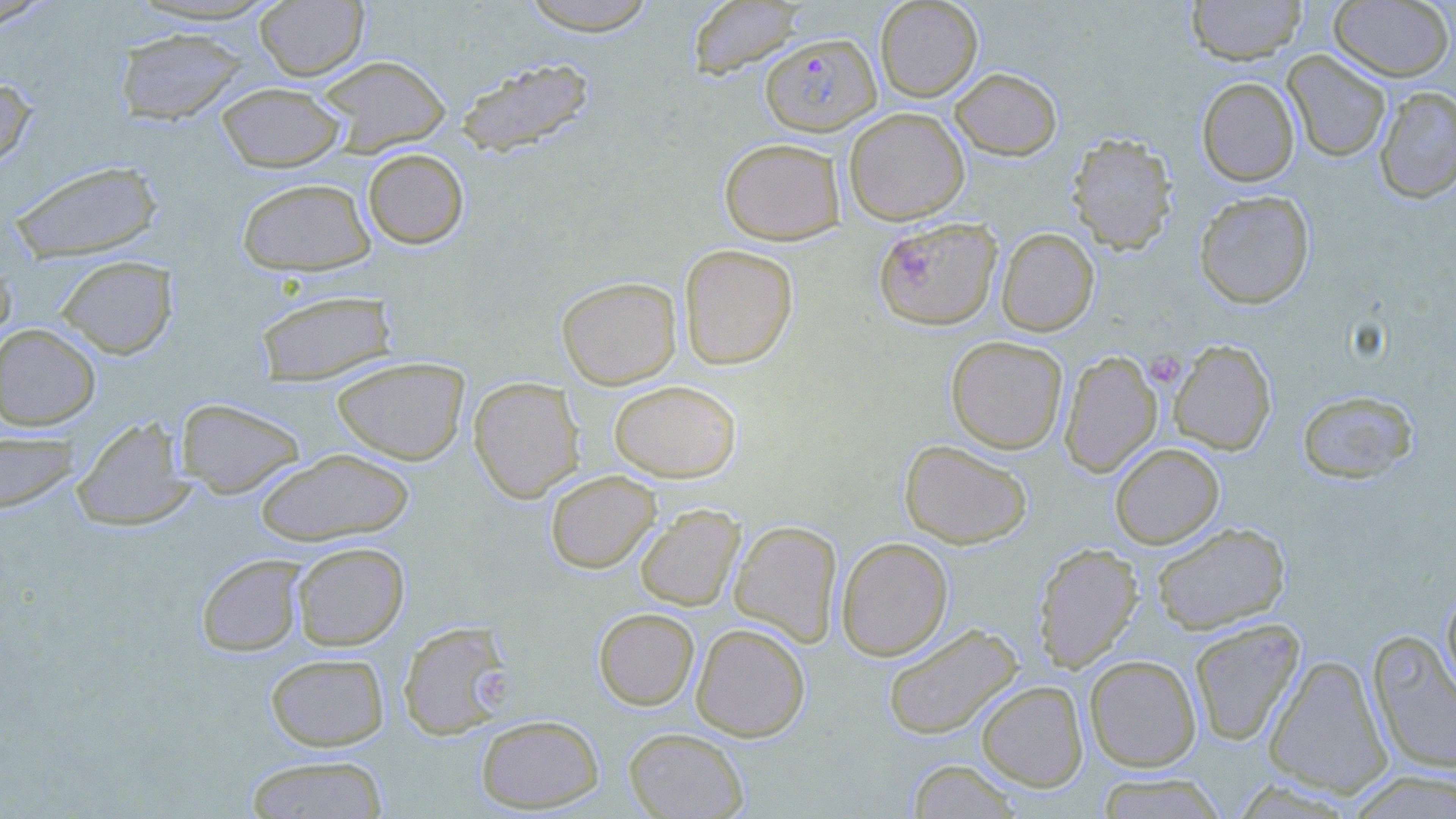

slide-level diagnosis = Plasmodium falciparum
stain = May-Grünwald-Giemsa
image size = 1456×819 pixels
uninfected red blood cell locations = approximate bounding boxes as named x1/y1/x2/y2 corners in pixels: (x1=517, y1=0, x2=659, y2=35), (x1=875, y1=0, x2=983, y2=102), (x1=1186, y1=0, x2=1307, y2=64), (x1=1329, y1=0, x2=1454, y2=82), (x1=255, y1=1, x2=369, y2=81), (x1=687, y1=1, x2=802, y2=79), (x1=0, y1=3, x2=55, y2=34), (x1=114, y1=28, x2=249, y2=125), (x1=1283, y1=50, x2=1391, y2=163), (x1=316, y1=55, x2=451, y2=156), (x1=454, y1=56, x2=596, y2=158), (x1=949, y1=67, x2=1062, y2=161), (x1=0, y1=75, x2=37, y2=174), (x1=1197, y1=77, x2=1299, y2=186), (x1=216, y1=82, x2=346, y2=172), (x1=1374, y1=86, x2=1456, y2=204), (x1=844, y1=107, x2=970, y2=225), (x1=1067, y1=132, x2=1177, y2=254), (x1=719, y1=137, x2=846, y2=244), (x1=362, y1=147, x2=469, y2=249), (x1=7, y1=160, x2=162, y2=263), (x1=236, y1=177, x2=376, y2=276), (x1=1193, y1=190, x2=1314, y2=309), (x1=873, y1=217, x2=1002, y2=330), (x1=996, y1=227, x2=1099, y2=337), (x1=678, y1=244, x2=798, y2=370), (x1=55, y1=255, x2=178, y2=359), (x1=0, y1=256, x2=15, y2=353), (x1=556, y1=276, x2=682, y2=390), (x1=254, y1=288, x2=398, y2=387), (x1=0, y1=323, x2=101, y2=431), (x1=945, y1=335, x2=1068, y2=454), (x1=1168, y1=339, x2=1276, y2=455), (x1=1059, y1=350, x2=1163, y2=477), (x1=332, y1=357, x2=469, y2=465), (x1=468, y1=376, x2=585, y2=503), (x1=608, y1=380, x2=741, y2=482), (x1=1297, y1=390, x2=1418, y2=484), (x1=175, y1=397, x2=306, y2=499), (x1=72, y1=416, x2=194, y2=531), (x1=0, y1=431, x2=79, y2=514), (x1=899, y1=439, x2=1033, y2=549), (x1=1110, y1=443, x2=1224, y2=549), (x1=255, y1=448, x2=415, y2=546), (x1=545, y1=470, x2=661, y2=574), (x1=635, y1=504, x2=744, y2=612), (x1=729, y1=520, x2=843, y2=647), (x1=1150, y1=522, x2=1290, y2=635), (x1=836, y1=536, x2=953, y2=661), (x1=291, y1=541, x2=409, y2=651), (x1=1033, y1=542, x2=1144, y2=672), (x1=195, y1=554, x2=307, y2=657), (x1=1441, y1=585, x2=1456, y2=700), (x1=593, y1=607, x2=700, y2=710), (x1=1188, y1=618, x2=1305, y2=746), (x1=397, y1=620, x2=511, y2=740), (x1=691, y1=623, x2=811, y2=742), (x1=882, y1=623, x2=1023, y2=740), (x1=1367, y1=632, x2=1456, y2=775), (x1=265, y1=652, x2=389, y2=752), (x1=1084, y1=654, x2=1201, y2=772), (x1=1264, y1=654, x2=1392, y2=797), (x1=976, y1=680, x2=1088, y2=792), (x1=475, y1=714, x2=605, y2=813), (x1=624, y1=727, x2=749, y2=818), (x1=243, y1=755, x2=390, y2=818), (x1=906, y1=759, x2=1022, y2=818), (x1=1345, y1=769, x2=1456, y2=818), (x1=1095, y1=773, x2=1227, y2=818)
magnification = 1000x
Plasmodium falciparum-infected red blood cell locations = approximate bounding boxes as named x1/y1/x2/y2 corners in pixels: (x1=761, y1=32, x2=881, y2=136)
modality = light microscopy
platelet locations = approximate bounding boxes as named x1/y1/x2/y2 corners in pixels: (x1=1145, y1=349, x2=1186, y2=388), (x1=477, y1=667, x2=513, y2=714)
field of view = one of a larger specimen
preparation = thin blood film